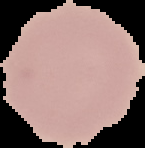

From a thin blood film. The area outside the segmented cell region is set to black. Image is 145×148 pixels. Malaria status: uninfected.